Assess this cell for malaria.
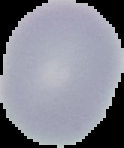
Uninfected.

Summary:
  - Image type: cell region segmented out of the field of view; surrounding area masked to black
  - Preparation: thin blood smear
  - Image size: 124×148 pixels